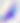

modality = photomicrograph
magnification = 400x
identification = Toxoplasma gondii